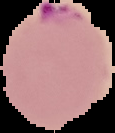 Segmented cell region on a black background. From a thin blood smear. Image is 115×133 pixels. Result: malaria parasites identified.